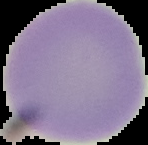
Malaria status: uninfected. The area outside the segmented cell region is set to black. Image is 148×145 pixels. From a thin blood smear.